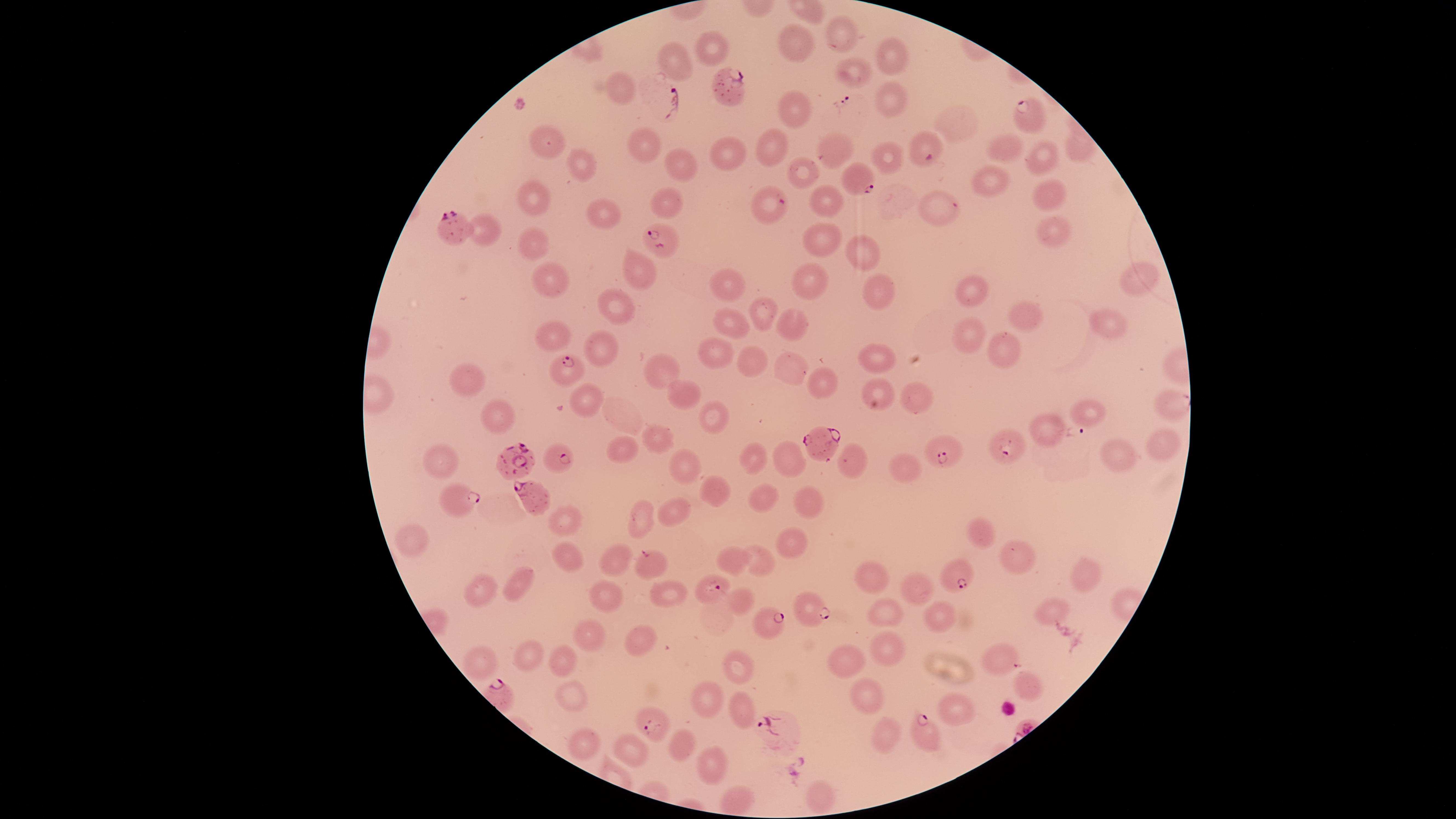

presence = malaria parasites seen
field of view = single
capture = smartphone photograph through the microscope eyepiece
uninfected RBCs = approximate marker points as [x, y] in pixels: [847, 32], [800, 44], [708, 50], [896, 54], [672, 64], [853, 70], [620, 91], [891, 101], [790, 111], [953, 124], [541, 143], [642, 146], [1005, 146], [772, 147], [1043, 151], [729, 153], [829, 153], [884, 154], [581, 163], [675, 164], [806, 165], [992, 183], [1047, 187], [824, 198], [529, 200], [668, 205], [938, 207], [602, 214], [485, 221], [1056, 225], [823, 239], [531, 245], [864, 252], [635, 269], [550, 279], [810, 279], [1134, 281], [723, 286], [878, 292], [981, 295], [619, 300], [763, 312], [1024, 314], [1112, 324], [788, 326], [730, 330], [966, 335], [555, 338], [602, 342], [996, 348], [714, 361], [755, 361], [877, 361], [662, 369], [793, 370], [472, 380], [822, 382], [915, 395], [585, 396], [681, 396], [712, 414], [1086, 414], [498, 417], [659, 440], [1161, 440], [621, 453], [1119, 457], [753, 459], [791, 459], [441, 463], [857, 464], [906, 470], [682, 471], [717, 491], [764, 497], [809, 498], [675, 508], [642, 511], [560, 520], [985, 536], [793, 538], [414, 540], [566, 551], [612, 554], [734, 555], [1018, 555], [763, 559], [1086, 569], [870, 570], [514, 579], [910, 589], [479, 593], [667, 594], [740, 598], [611, 601], [1051, 612], [887, 613], [939, 613], [592, 637], [643, 649], [530, 651], [887, 654], [1003, 659], [479, 660], [559, 660], [848, 664], [738, 672], [1026, 686], [574, 699], [704, 701], [865, 701], [738, 708], [955, 713], [891, 734], [587, 744], [676, 748], [628, 749], [713, 765], [823, 794], [734, 800]
stain = Giemsa
image size = 1456×819 pixels
preparation = thin blood smear
species = Plasmodium falciparum
visible region = circular
parasitized RBCs = approximate marker points as [x, y] in pixels: [728, 87], [1025, 118], [926, 151], [863, 180], [770, 205], [458, 236], [655, 242], [565, 367], [821, 447], [1008, 447], [946, 455], [562, 458], [521, 460], [535, 499], [457, 501], [648, 560], [952, 578], [712, 587], [808, 609], [766, 626], [650, 723], [926, 735]